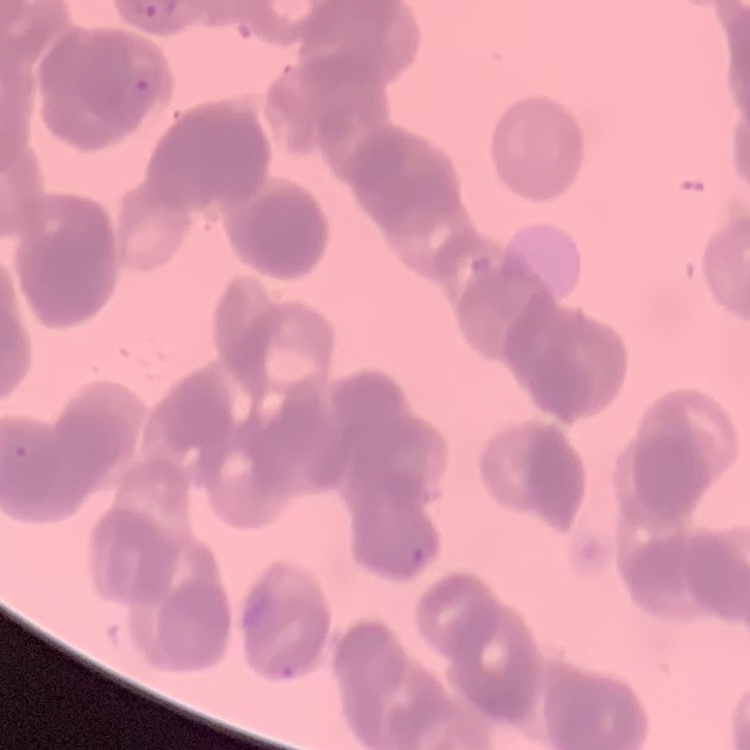
The erythrocytes exhibit rouleaux formation. Thin blood film. One tile cut from a larger photomicrograph. Stained with either Field's or Giemsa.